Classify this cell by malaria status.
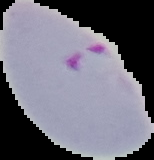
Parasitized.

From a thin blood smear. Image is 154×160 pixels. The area outside the segmented cell region is set to black.